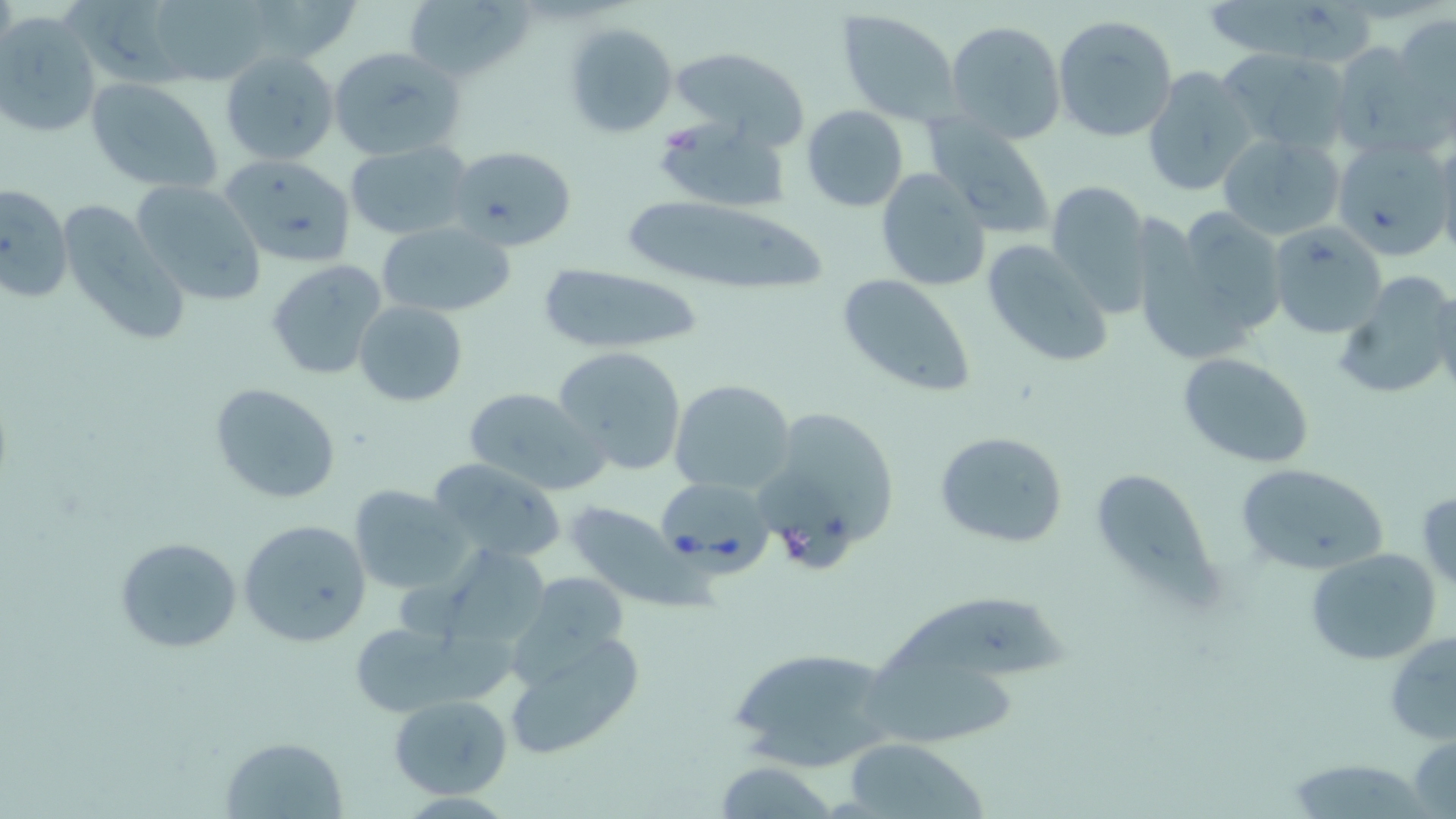

Approximate bounding boxes as (x1, y1, x2, y2) in pixels. Uninfected red blood cell locations: (262, 0, 366, 61), (404, 0, 526, 85), (62, 1, 187, 86), (1204, 1, 1384, 61), (141, 2, 274, 87), (838, 11, 959, 126), (0, 12, 102, 140), (1392, 13, 1455, 129), (1052, 14, 1178, 142), (946, 20, 1066, 144), (561, 21, 679, 140), (1327, 41, 1449, 158), (328, 45, 465, 162), (668, 46, 811, 144), (1219, 47, 1352, 156), (219, 50, 339, 166), (1141, 67, 1258, 197), (85, 78, 225, 192), (801, 104, 910, 212), (650, 117, 791, 212), (926, 119, 1056, 239), (1217, 132, 1346, 241), (1332, 136, 1452, 262), (1437, 137, 1456, 269), (343, 140, 474, 241), (447, 143, 578, 251), (216, 154, 357, 268), (875, 168, 991, 292), (132, 179, 266, 305), (1046, 179, 1153, 315), (0, 183, 72, 303), (616, 194, 830, 301), (65, 201, 188, 348), (1141, 205, 1289, 363), (376, 219, 515, 319), (1269, 222, 1385, 338), (980, 238, 1114, 369), (265, 260, 387, 381), (534, 262, 710, 355), (1331, 270, 1456, 405), (836, 273, 980, 401), (353, 300, 469, 407), (552, 346, 689, 476), (1176, 352, 1317, 470), (670, 380, 796, 495), (209, 382, 342, 506), (460, 386, 604, 495), (753, 404, 902, 568), (934, 429, 1069, 550), (425, 458, 569, 567), (1233, 462, 1388, 578), (1087, 465, 1217, 603), (350, 486, 470, 594), (1415, 486, 1456, 592), (560, 501, 701, 606), (238, 517, 371, 646), (113, 536, 244, 654), (1303, 547, 1441, 666), (442, 549, 554, 686), (503, 574, 634, 697), (872, 588, 1071, 685), (345, 619, 477, 719), (498, 622, 643, 764), (1385, 631, 1456, 744), (731, 644, 896, 773), (857, 655, 1030, 750), (389, 695, 513, 800), (1408, 732, 1456, 817), (220, 737, 348, 818), (843, 739, 986, 817), (1283, 759, 1433, 817), (712, 761, 840, 818). Babesia divergens-infected red blood cell locations: (654, 476, 773, 570). Slide-level diagnosis: Babesia divergens. Image is 1456×819 pixels. Captured at 1000x magnification. Optical microscopy. Thin blood smear. Single field of view. May-Grünwald-Giemsa stain.